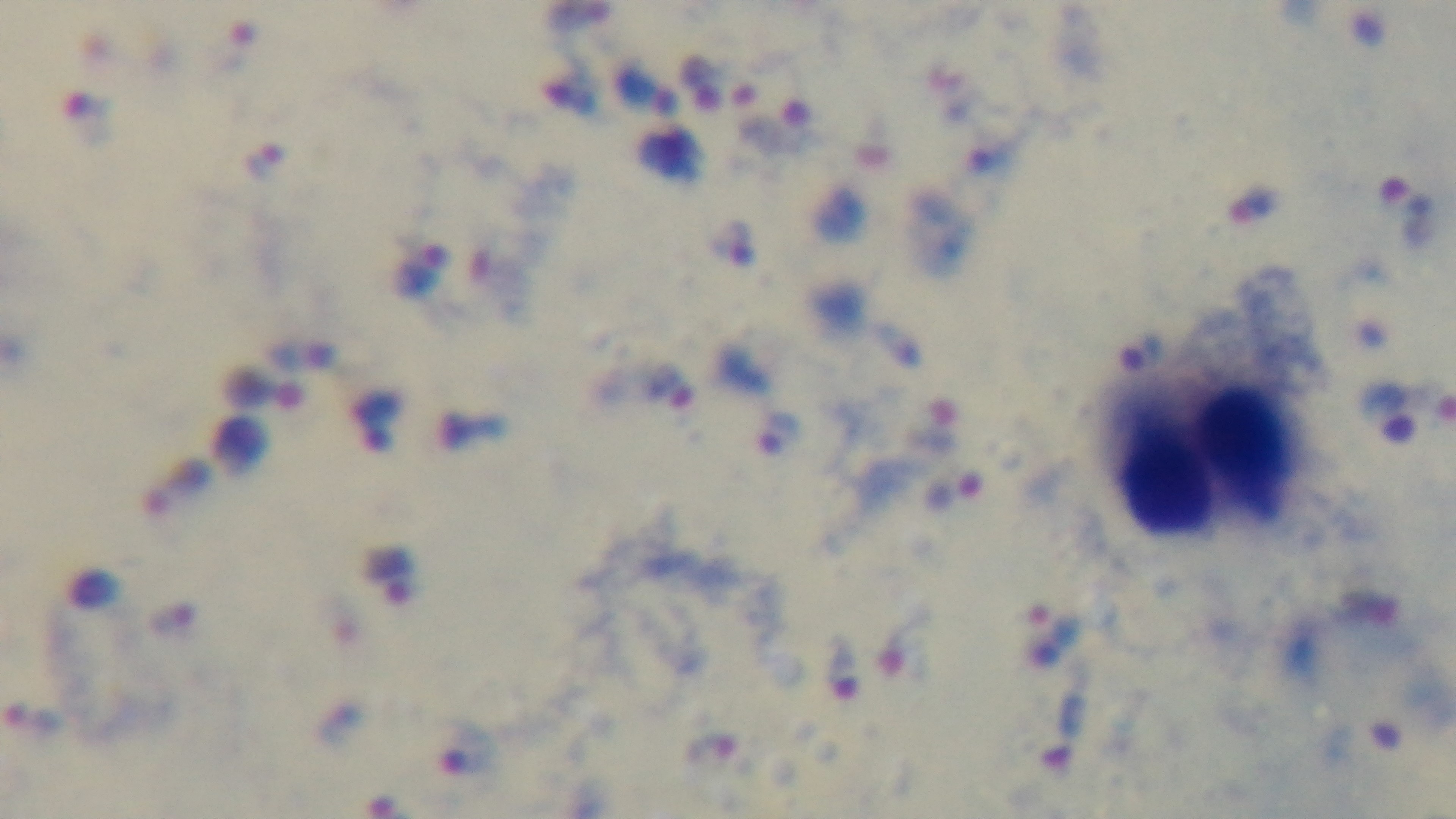

objective = 100x oil immersion
capture = mounted 4K digital camera
preparation = thick smear
malaria status = infected
field of view = single
modality = light microscopy
stain = Giemsa